Identify the blood parasite species.
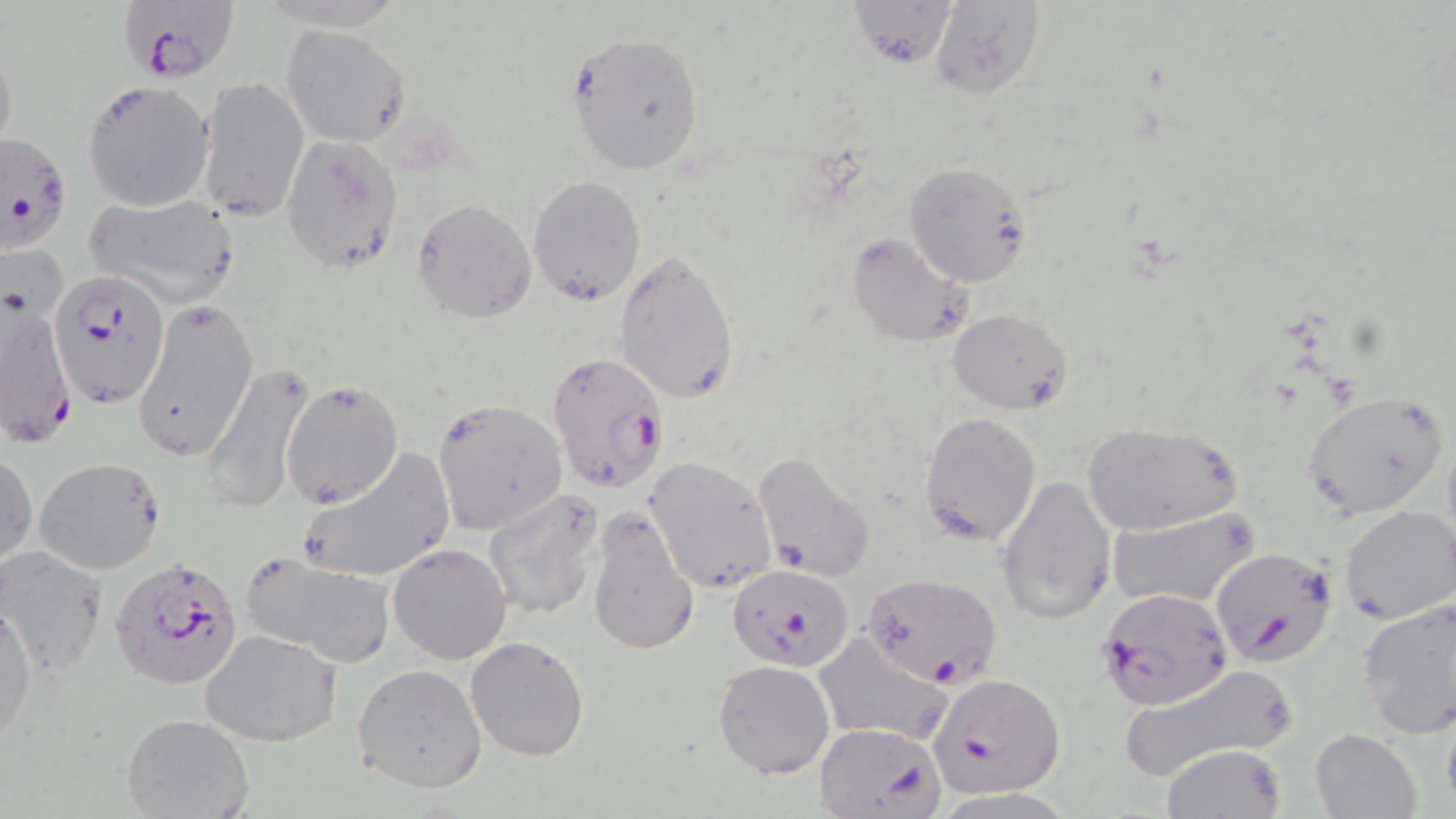
Plasmodium falciparum.

Approximate bounding boxes as (x1,y1)-(x2,y2) corner pairs in pixels. Plasmodium falciparum-infected red blood cell locations (subset): (122,1)-(246,85), (0,131)-(71,254), (52,269)-(170,406), (1,290)-(76,445), (546,349)-(670,496), (1209,544)-(1338,667), (108,557)-(242,694), (727,563)-(853,670), (1095,587)-(1234,711), (931,674)-(1067,797), (814,721)-(947,818). Uninfected red blood cell locations (subset): (843,0)-(959,69), (929,1)-(1049,100), (282,23)-(409,146), (566,31)-(706,177), (0,36)-(19,164), (195,76)-(309,223), (83,80)-(213,211), (281,134)-(402,272), (902,162)-(1033,287), (527,176)-(647,306), (83,193)-(243,308), (412,198)-(536,323), (846,231)-(972,348), (615,250)-(741,406), (133,298)-(259,463), (948,307)-(1072,415), (201,362)-(316,514), (280,376)-(403,507), (1301,391)-(1451,520), (432,399)-(568,536), (918,410)-(1041,547), (1081,419)-(1242,535), (298,447)-(454,585), (1,450)-(37,572), (752,452)-(877,582), (646,456)-(777,593), (34,457)-(166,574), (997,473)-(1115,622), (481,488)-(606,622), (1337,504)-(1456,624), (586,507)-(701,657), (1107,508)-(1259,609), (389,542)-(512,666), (0,546)-(109,677), (241,551)-(397,668), (1355,596)-(1456,737), (1,597)-(36,748), (200,629)-(343,747), (812,631)-(954,743), (465,635)-(590,761), (712,660)-(835,778), (1116,661)-(1300,781), (353,663)-(489,793), (120,713)-(255,819), (1310,728)-(1420,818), (1160,744)-(1287,818). Thin blood smear. May-Grünwald-Giemsa stain. 1000x magnification. Image is 1456×819 pixels. Light microscopy. One field of a larger specimen.